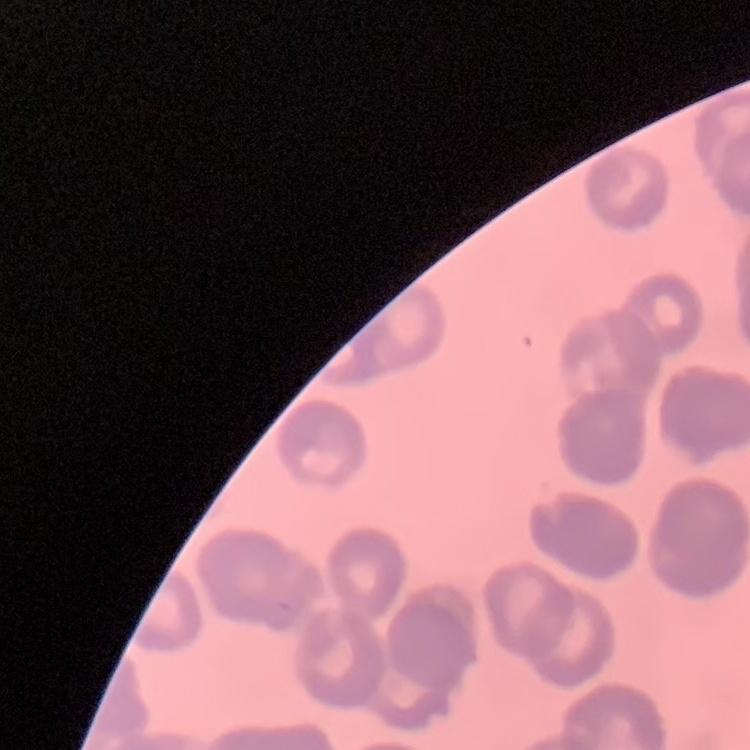
{
  "erythrocyte_morphology": "rouleaux formation",
  "stain": "Field's or Giemsa",
  "image_type": "square crop of a larger photomicrograph",
  "preparation": "thin blood film"
}